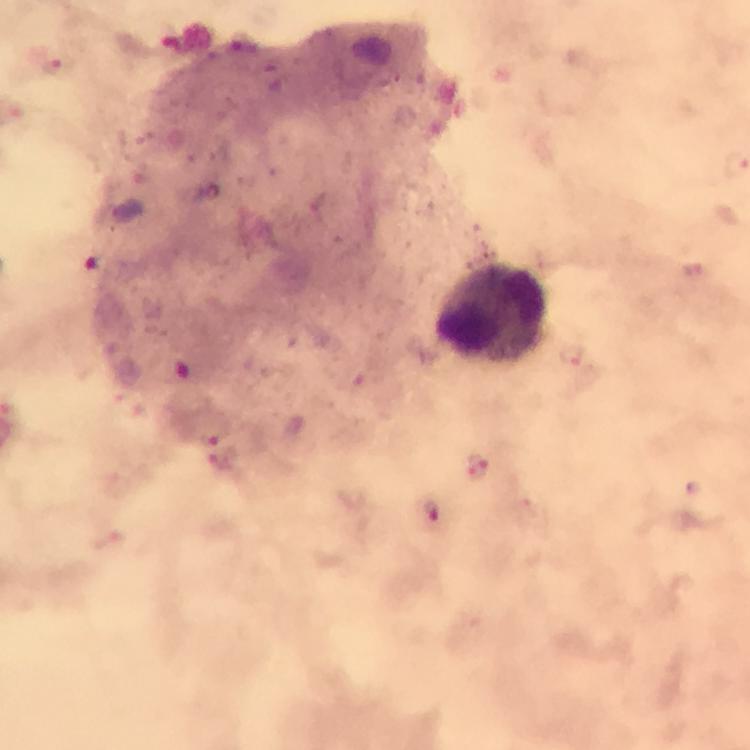
cropped from = one field of view
capture = smartphone camera through the microscope
magnification = 100x
stain = Giemsa
image size = 750×750 pixels
immersion oil = applied
malaria parasite locations = approximate object centers, in pixels from the top-left corner: (x=246, y=44), (x=58, y=70), (x=99, y=265), (x=692, y=271), (x=191, y=373), (x=215, y=433), (x=226, y=460), (x=479, y=467)
preparation = thick blood film
context = from a diagnostic examination for malaria
leukocyte locations = approximate object centers, in pixels from the top-left corner: (x=493, y=313)